Name the cell type shown.
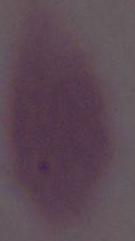

This is an erythrocyte.

magnification = 1000x
modality = micrograph